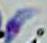
{
  "modality": "micrograph",
  "identification": "Toxoplasma gondii",
  "magnification": "1000x"
}